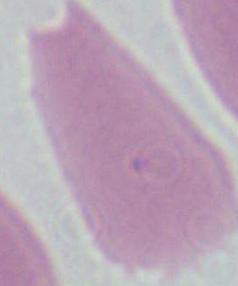
Photomicrograph. 1000x magnification. An erythrocyte is seen.